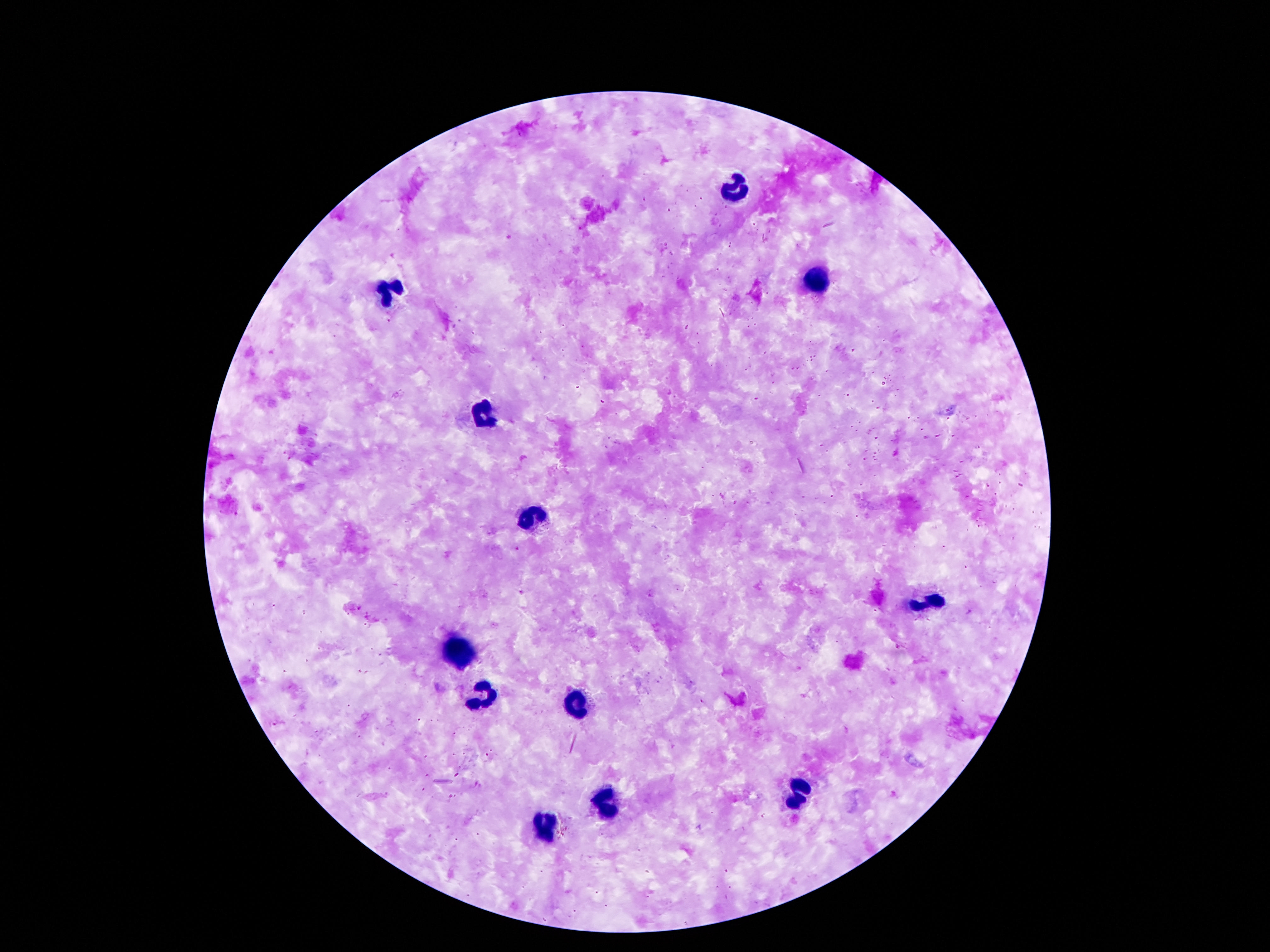

field of view = single
patient malaria status = not infected
leukocyte locations = approximate centers as [x, y] in pixels: [731, 186], [815, 281], [386, 289], [487, 412], [535, 514], [926, 604], [453, 649], [483, 696], [576, 704], [797, 793], [604, 801], [547, 824]
preparation = thick blood film
capture = smartphone camera through the microscope eyepiece
image size = 1270×952 pixels
stain = Giemsa
magnification = 100x